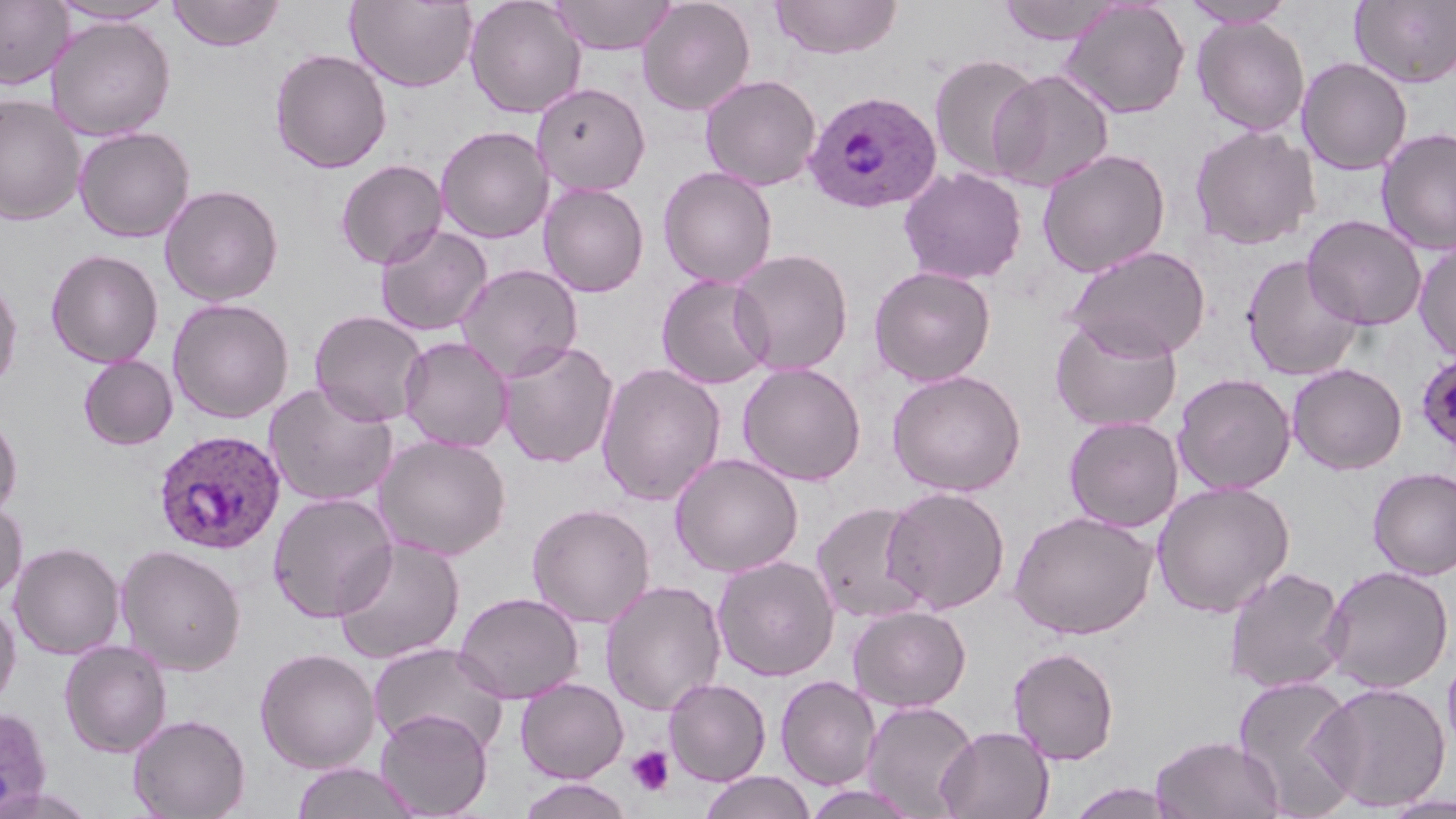
{
  "slide_level_diagnosis": "Plasmodium ovale",
  "modality": "light microscopy",
  "magnification": "1000x",
  "preparation": "thin blood film",
  "plasmodium_ovale_infected_red_blood_cell_locations": "approximate bounding boxes as (x1,y1)-(x2,y2) corner pairs in pixels: (805,90)-(942,214), (1415,350)-(1456,457), (153,429)-(286,555), (0,705)-(53,818)",
  "platelet_locations": "approximate bounding boxes as (x1,y1)-(x2,y2) corner pairs in pixels: (627,746)-(674,796)",
  "uninfected_red_blood_cell_locations": "approximate bounding boxes as (x1,y1)-(x2,y2) corner pairs in pixels: (48,0)-(177,25), (167,0)-(285,51), (465,0)-(586,119), (548,0)-(678,55), (637,0)-(756,116), (769,0)-(903,60), (996,0)-(1124,45), (1059,0)-(1191,119), (1180,0)-(1297,28), (1350,0)-(1456,88), (0,1)-(73,89), (346,1)-(477,92), (46,16)-(176,141), (1193,17)-(1310,136), (269,48)-(393,174), (928,53)-(1044,182), (1296,57)-(1413,176), (988,69)-(1115,193), (700,74)-(822,191), (532,82)-(651,196), (0,94)-(86,225), (1189,124)-(1320,250), (435,125)-(554,244), (73,126)-(195,243), (1376,127)-(1456,255), (1037,149)-(1171,278), (335,159)-(448,270), (658,166)-(778,288), (898,167)-(1027,285), (538,182)-(649,298), (159,183)-(284,306), (1302,214)-(1427,330), (374,224)-(493,337), (1413,240)-(1456,362), (1063,245)-(1212,361), (45,248)-(164,367), (728,248)-(854,376), (1241,254)-(1364,381), (455,263)-(583,383), (868,265)-(996,387), (656,274)-(773,389), (0,275)-(23,393), (167,297)-(295,423), (309,309)-(429,427), (1050,313)-(1183,433), (399,336)-(513,453), (497,340)-(620,468), (78,355)-(178,451), (595,362)-(726,506), (737,362)-(866,486), (1287,363)-(1407,475), (887,369)-(1026,497), (1173,373)-(1296,495), (263,382)-(399,507), (0,412)-(23,520), (1063,415)-(1184,533), (373,434)-(511,560), (669,453)-(803,578), (1368,467)-(1456,579), (1151,481)-(1296,618), (882,485)-(1011,614), (266,491)-(399,622), (0,498)-(28,603), (810,500)-(932,623), (526,503)-(656,628), (1007,511)-(1157,639), (331,537)-(466,664), (9,541)-(125,659), (115,544)-(247,675), (712,555)-(839,682), (1224,565)-(1349,693), (1321,565)-(1454,693), (600,579)-(727,716), (453,591)-(584,704), (0,599)-(21,710), (848,605)-(971,712), (58,639)-(173,758), (368,642)-(509,754), (1007,645)-(1120,765), (254,647)-(380,773), (1442,648)-(1456,760), (1233,674)-(1363,816), (775,675)-(880,790), (514,677)-(629,783), (663,678)-(771,786), (1315,680)-(1451,812), (861,700)-(979,819), (374,709)-(493,818), (127,713)-(251,819), (935,725)-(1054,819), (1150,734)-(1286,819), (290,762)-(421,819), (699,771)-(816,819), (518,777)-(635,819), (1065,783)-(1183,818), (802,784)-(923,819), (1378,793)-(1456,819)",
  "field_of_view": "one of a larger specimen",
  "image_size": "1456×819 pixels",
  "stain": "May-Grünwald-Giemsa"
}